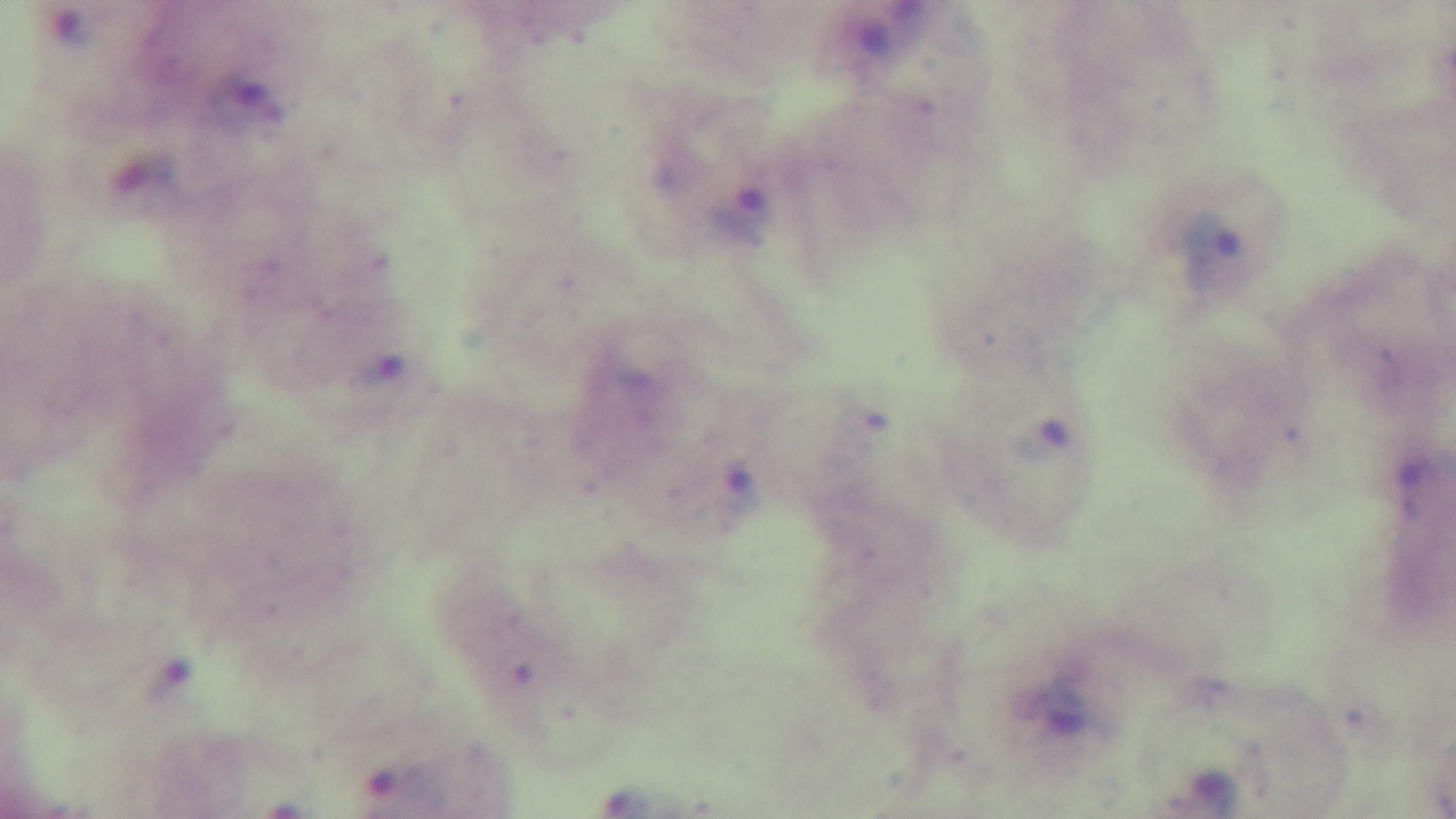
Summary:
  - Field of view: one from the slide
  - Objective: 100x oil immersion
  - Preparation: thick blood film
  - Stain: Giemsa
  - Malaria status: infected
  - Modality: light microscopy
  - Capture: mounted 4K digital camera